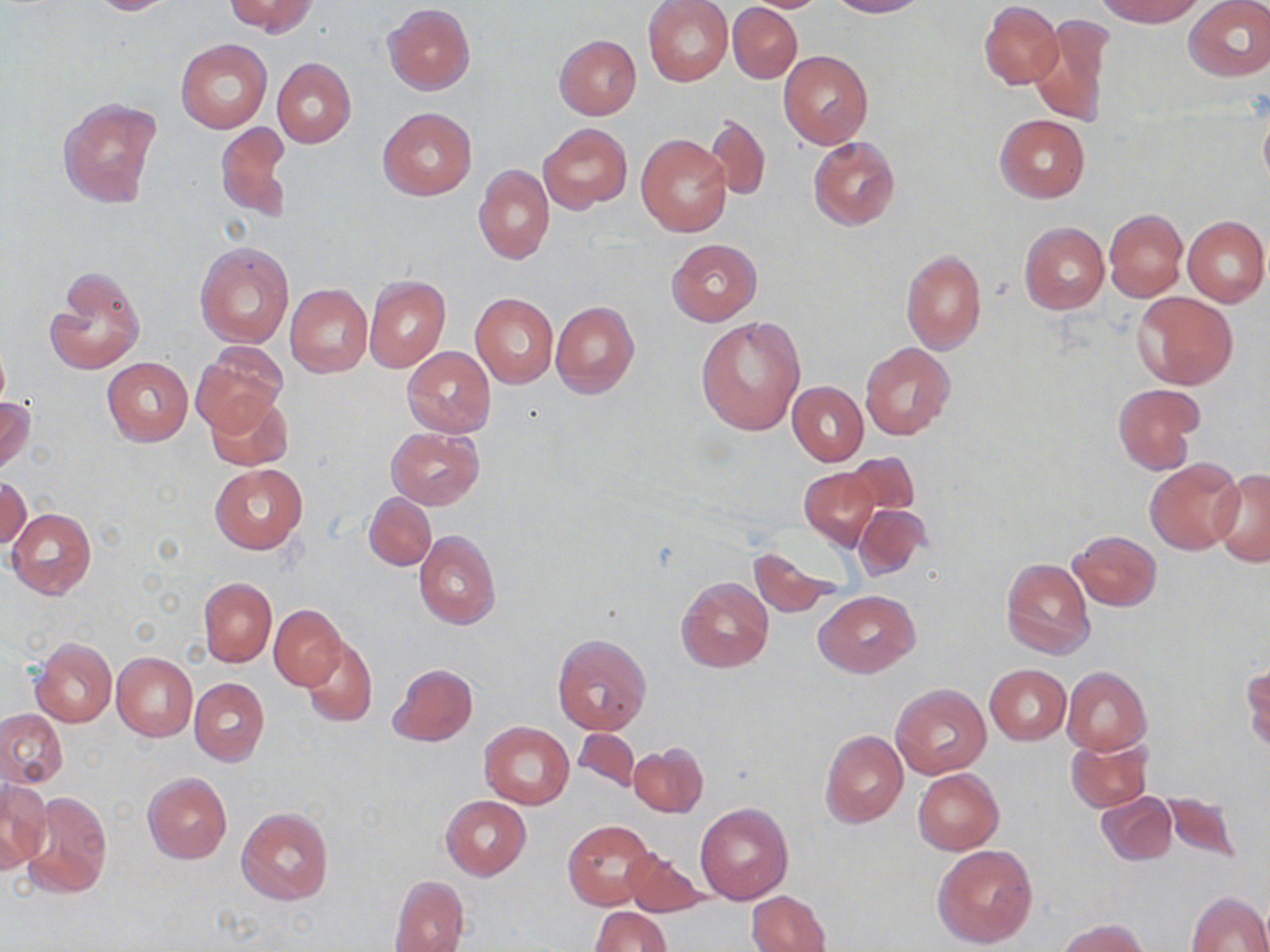
Summary:
  - Coordinate format: approximate bounding boxes as named x1/y1/x2/y2 corners in pixels
  - Uninfected red blood cell locations: (x1=83, y1=0, x2=180, y2=15), (x1=227, y1=0, x2=317, y2=36), (x1=643, y1=0, x2=733, y2=87), (x1=740, y1=0, x2=833, y2=12), (x1=828, y1=0, x2=927, y2=17), (x1=1096, y1=0, x2=1204, y2=25), (x1=1185, y1=0, x2=1270, y2=82), (x1=980, y1=1, x2=1062, y2=88), (x1=383, y1=3, x2=475, y2=94), (x1=728, y1=3, x2=802, y2=83), (x1=1030, y1=15, x2=1114, y2=127), (x1=555, y1=35, x2=642, y2=120), (x1=177, y1=39, x2=270, y2=133), (x1=779, y1=51, x2=874, y2=149), (x1=272, y1=58, x2=356, y2=148), (x1=58, y1=98, x2=161, y2=208), (x1=1258, y1=105, x2=1270, y2=194), (x1=377, y1=106, x2=477, y2=200), (x1=995, y1=114, x2=1091, y2=202), (x1=704, y1=115, x2=771, y2=200), (x1=217, y1=122, x2=291, y2=223), (x1=539, y1=122, x2=631, y2=212), (x1=637, y1=135, x2=733, y2=237), (x1=809, y1=136, x2=900, y2=231), (x1=474, y1=165, x2=554, y2=264), (x1=1104, y1=209, x2=1187, y2=300), (x1=1182, y1=215, x2=1269, y2=307), (x1=1019, y1=222, x2=1109, y2=313), (x1=666, y1=238, x2=762, y2=326), (x1=194, y1=240, x2=296, y2=349), (x1=900, y1=249, x2=986, y2=356), (x1=46, y1=267, x2=144, y2=375), (x1=364, y1=274, x2=450, y2=373), (x1=285, y1=284, x2=373, y2=377), (x1=1133, y1=290, x2=1238, y2=389), (x1=470, y1=292, x2=558, y2=387), (x1=550, y1=301, x2=640, y2=399), (x1=695, y1=316, x2=807, y2=435), (x1=192, y1=343, x2=286, y2=431), (x1=861, y1=343, x2=955, y2=441), (x1=403, y1=346, x2=495, y2=437), (x1=102, y1=357, x2=193, y2=446), (x1=788, y1=382, x2=868, y2=465), (x1=1113, y1=384, x2=1202, y2=474), (x1=203, y1=393, x2=293, y2=470), (x1=0, y1=395, x2=35, y2=475), (x1=386, y1=427, x2=483, y2=509), (x1=842, y1=452, x2=920, y2=518), (x1=1145, y1=458, x2=1243, y2=554), (x1=210, y1=464, x2=307, y2=552), (x1=799, y1=467, x2=880, y2=550), (x1=1210, y1=469, x2=1270, y2=567), (x1=1, y1=477, x2=30, y2=550), (x1=364, y1=493, x2=437, y2=571), (x1=853, y1=503, x2=931, y2=581), (x1=7, y1=507, x2=96, y2=599), (x1=413, y1=530, x2=501, y2=629), (x1=1069, y1=531, x2=1161, y2=611), (x1=749, y1=545, x2=844, y2=617), (x1=1000, y1=556, x2=1095, y2=659), (x1=676, y1=576, x2=773, y2=672), (x1=199, y1=577, x2=276, y2=667), (x1=814, y1=591, x2=920, y2=676), (x1=269, y1=605, x2=345, y2=689), (x1=552, y1=634, x2=651, y2=734), (x1=301, y1=635, x2=378, y2=727), (x1=32, y1=637, x2=117, y2=727), (x1=111, y1=652, x2=198, y2=740), (x1=388, y1=663, x2=478, y2=746), (x1=1242, y1=663, x2=1270, y2=752), (x1=985, y1=664, x2=1070, y2=744), (x1=1062, y1=667, x2=1150, y2=753), (x1=189, y1=677, x2=269, y2=766), (x1=891, y1=684, x2=990, y2=779), (x1=0, y1=708, x2=67, y2=787), (x1=480, y1=721, x2=575, y2=808), (x1=572, y1=729, x2=639, y2=792), (x1=820, y1=730, x2=907, y2=828), (x1=1067, y1=736, x2=1152, y2=813), (x1=629, y1=742, x2=707, y2=818), (x1=913, y1=768, x2=1003, y2=854), (x1=142, y1=773, x2=231, y2=863), (x1=1, y1=781, x2=50, y2=874), (x1=20, y1=789, x2=113, y2=901), (x1=1157, y1=790, x2=1244, y2=862), (x1=1096, y1=791, x2=1176, y2=866), (x1=441, y1=796, x2=531, y2=880), (x1=695, y1=802, x2=793, y2=904), (x1=236, y1=806, x2=335, y2=906), (x1=562, y1=818, x2=658, y2=910), (x1=932, y1=845, x2=1038, y2=949), (x1=622, y1=850, x2=709, y2=917), (x1=389, y1=874, x2=470, y2=952), (x1=747, y1=890, x2=831, y2=952), (x1=1185, y1=890, x2=1270, y2=952), (x1=589, y1=906, x2=671, y2=952), (x1=1058, y1=918, x2=1152, y2=952)
  - Slide-level diagnosis: no evidence of blood parasites
  - Preparation: thin blood smear
  - Image size: 1270×952 pixels
  - Modality: light microscopy
  - Magnification: 1000x
  - Field of view: single
  - Stain: May-Grünwald-Giemsa